Assess this cell for malaria.
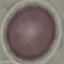
Uninfected.

Thin smear of blood. Cell patch, automatically extracted from a larger field of view and resized to 64 × 64 pixels. Giemsa-stained preparation. Photographed with a smartphone camera at the microscope eyepiece.